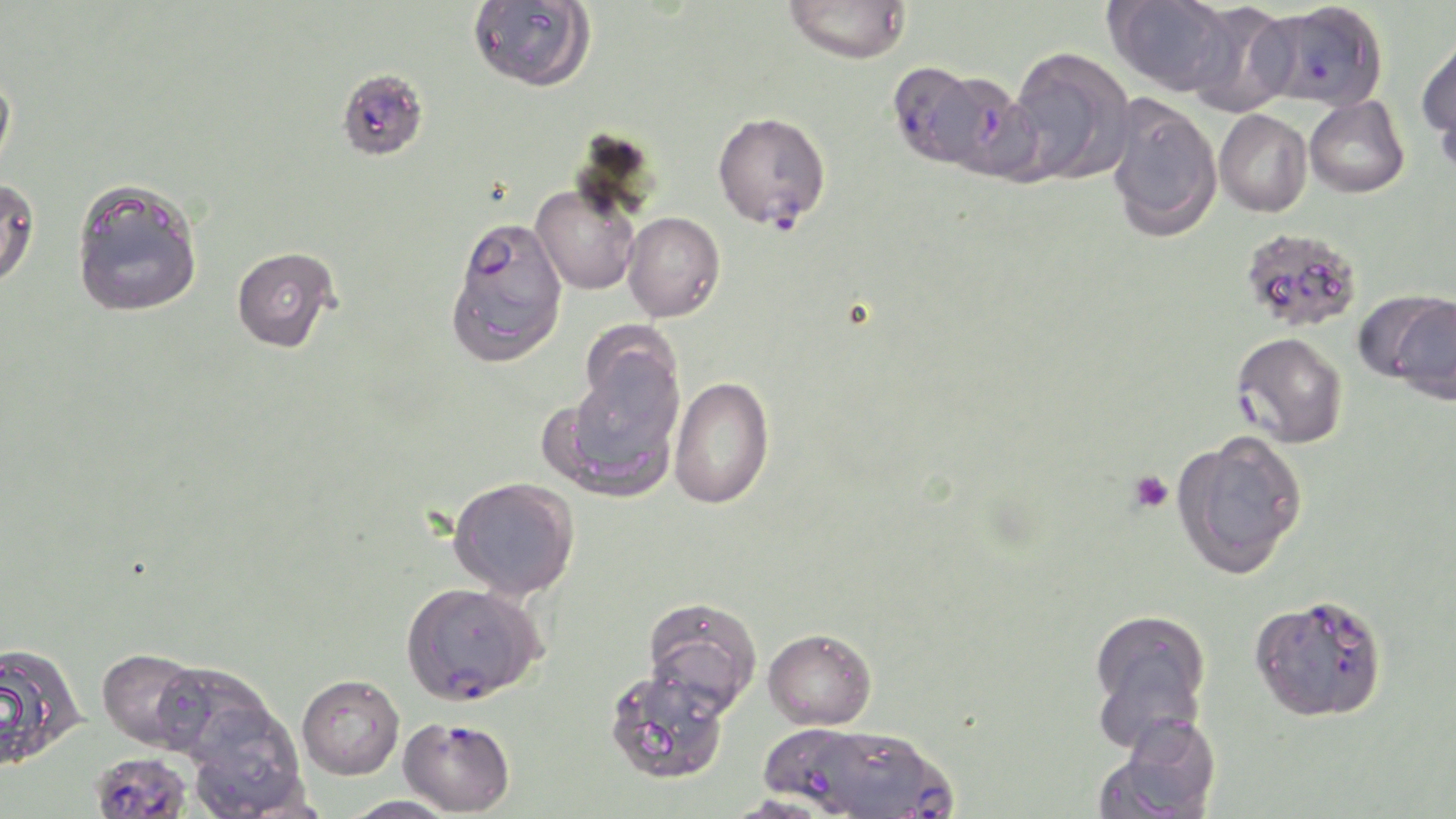
Approximate bounding boxes as [x1, y1, x2, y2] in pixels. Uninfected red blood cell locations: [783, 0, 913, 64], [1105, 0, 1237, 96], [468, 1, 596, 92], [1183, 3, 1299, 116], [1417, 33, 1456, 151], [1006, 46, 1135, 185], [0, 66, 17, 180], [1435, 73, 1456, 184], [1104, 94, 1222, 241], [1304, 96, 1410, 198], [1214, 109, 1312, 217], [0, 176, 40, 290], [70, 178, 203, 318], [531, 184, 640, 295], [622, 211, 725, 322], [1240, 227, 1363, 333], [232, 246, 340, 352], [448, 283, 565, 369], [1383, 292, 1456, 404], [553, 345, 686, 498], [668, 376, 775, 510], [1172, 431, 1309, 578], [447, 476, 580, 601], [641, 597, 763, 717], [1087, 608, 1213, 747], [763, 627, 877, 729], [0, 642, 86, 771], [97, 647, 212, 751], [150, 661, 281, 766], [603, 668, 730, 786], [297, 674, 404, 779], [183, 704, 309, 818], [1095, 717, 1222, 819], [761, 730, 865, 819], [339, 795, 462, 818]. Plasmodium falciparum-infected red blood cell locations: [1255, 2, 1389, 112], [889, 63, 1008, 172], [336, 68, 429, 161], [712, 110, 831, 230], [445, 217, 568, 332], [1231, 332, 1348, 448], [401, 580, 546, 704], [1250, 593, 1390, 723], [398, 716, 515, 816], [853, 735, 960, 818], [91, 754, 193, 819]. Platelet locations: [1127, 470, 1173, 514]. Slide-level diagnosis: Plasmodium falciparum. Single field of view. Thin blood smear. Image is 1456×819 pixels. May-Grünwald-Giemsa-stained preparation. Optical microscopy. Captured at 1000x magnification.